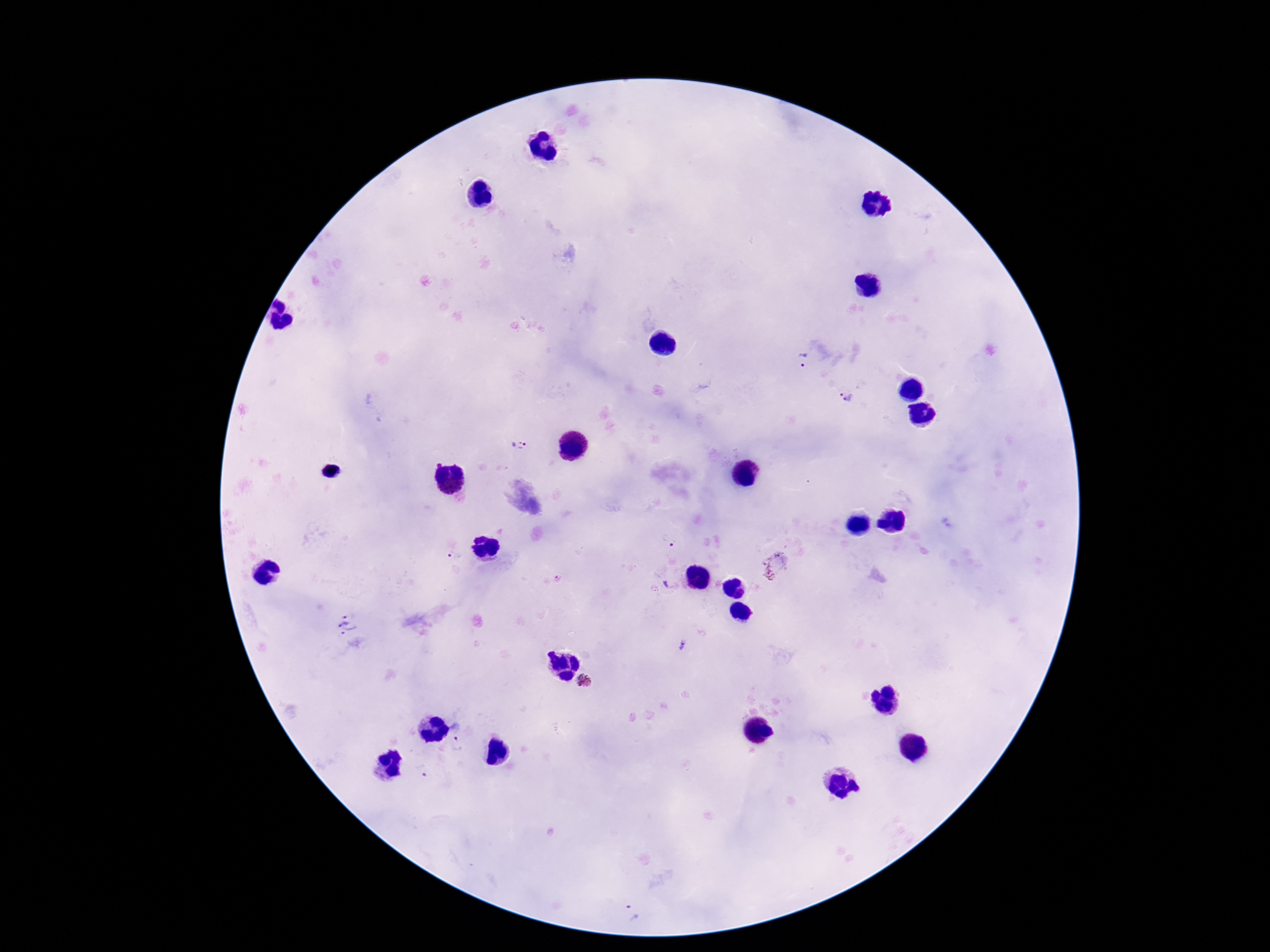

Approximate object centers, in pixels from the top-left corner. Plasmodium parasite locations: (x=802, y=360), (x=846, y=394), (x=520, y=447), (x=668, y=541), (x=455, y=557), (x=774, y=567), (x=666, y=585), (x=348, y=624), (x=681, y=645), (x=585, y=681), (x=458, y=734), (x=423, y=772), (x=632, y=912). Smartphone photograph taken through the microscope eyepiece. 100x magnification. Single field of view. Giemsa-stained preparation. Patient malaria status: infected. Thick blood smear. Image is 1270×952 pixels.